State the preparation type.
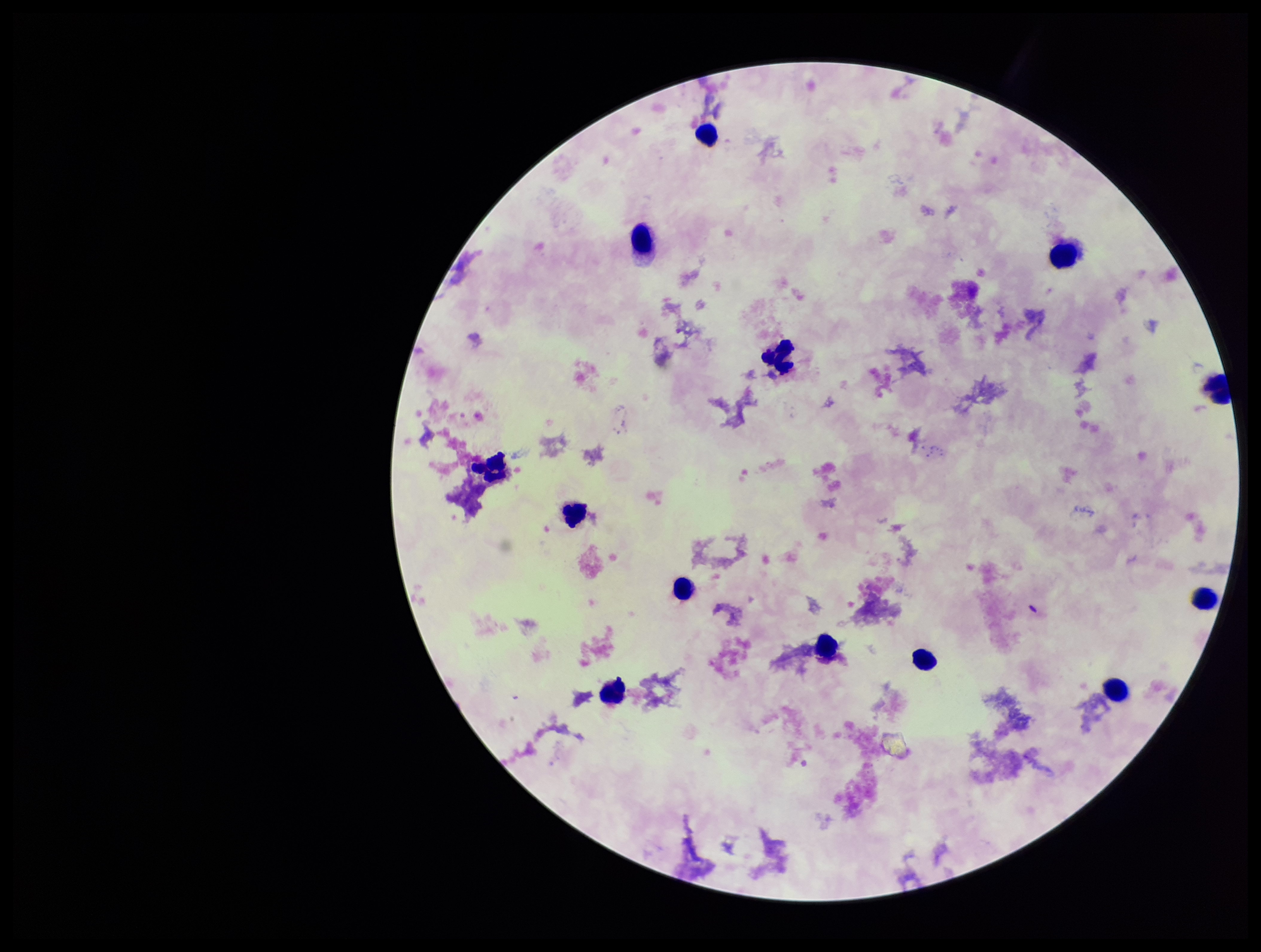

A thick smear.

Parasite count: 0. Patient malaria status: negative. One field from this slide. Plasmodium parasites: none identified. Stained with Giemsa. Smartphone photograph taken through the eyepiece of a microscope. Image is 1261×952 pixels. Leukocyte count: 13.